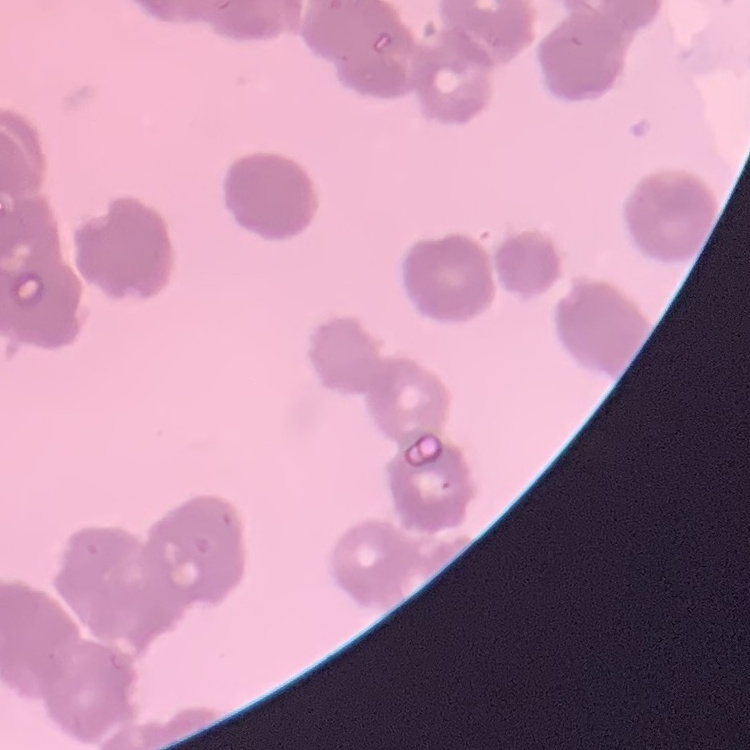

erythrocyte morphology = rouleaux formation
stain = Field's or Giemsa
preparation = thin blood film
image type = square crop of a larger photomicrograph